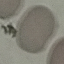

result = negative for malaria parasites
capture = smartphone camera at the microscope eyepiece
image type = automatically extracted cell patch, resized to 64 × 64 pixels
stain = Giemsa
preparation = thin blood film